Locate every blood parasite and identify its species.
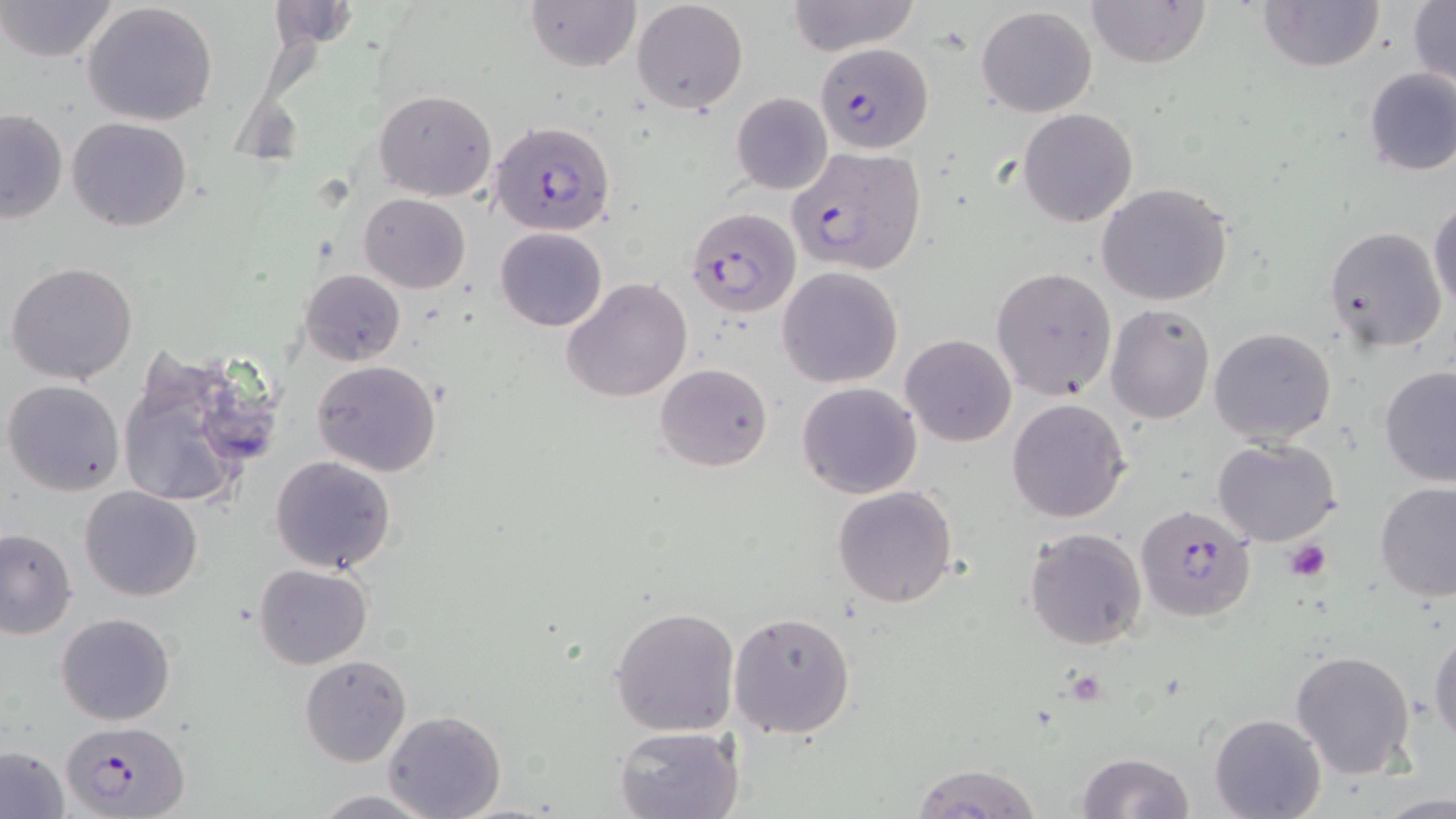

Approximate bounding boxes as (x1, y1, x2, y2) in pixels.
Plasmodium falciparum-infected red blood cells: (814, 42, 933, 152), (489, 120, 617, 236), (786, 145, 927, 274), (684, 205, 800, 318), (1135, 502, 1256, 623), (64, 719, 188, 818).
No Plasmodium ovale, Plasmodium malariae, Plasmodium vivax, Babesia divergens, or Trypanosoma brucei observed.

Uninfected red blood cell locations: (0, 0, 121, 65), (524, 0, 641, 72), (630, 0, 749, 117), (785, 0, 921, 56), (1085, 0, 1213, 68), (1257, 0, 1385, 73), (1407, 0, 1455, 91), (264, 1, 358, 52), (81, 2, 220, 128), (977, 5, 1097, 117), (1362, 67, 1456, 177), (373, 89, 497, 200), (730, 91, 834, 195), (0, 108, 69, 225), (1018, 109, 1138, 227), (67, 116, 193, 233), (1096, 182, 1234, 306), (358, 193, 471, 293), (1428, 199, 1456, 317), (1323, 226, 1448, 354), (494, 227, 607, 331), (6, 261, 138, 385), (777, 266, 903, 388), (990, 267, 1118, 400), (300, 268, 405, 366), (561, 278, 694, 405), (1105, 304, 1214, 424), (1208, 327, 1337, 447), (900, 334, 1016, 446), (116, 348, 268, 514), (312, 359, 442, 477), (655, 362, 773, 473), (1378, 364, 1456, 486), (3, 379, 126, 496), (796, 381, 922, 500), (1006, 399, 1130, 522), (1213, 439, 1342, 547), (269, 455, 397, 573), (1374, 482, 1456, 602), (832, 485, 960, 608), (80, 486, 202, 602), (1024, 527, 1147, 650), (0, 528, 76, 639), (253, 563, 375, 671), (609, 604, 741, 738), (729, 609, 856, 739), (56, 612, 177, 726), (1429, 624, 1456, 748), (1290, 648, 1415, 779), (299, 655, 412, 766), (384, 709, 506, 818), (1209, 712, 1326, 819), (613, 726, 741, 819), (1, 745, 69, 817), (1076, 751, 1197, 818), (907, 762, 1044, 818), (308, 790, 444, 818), (1374, 793, 1455, 817). Platelet locations: (1284, 540, 1332, 581). Slide-level diagnosis: Plasmodium falciparum. Image is 1456×819 pixels. 1000x magnification. Light microscopy. One field of a larger specimen. Thin blood smear. May-Grünwald-Giemsa-stained preparation.